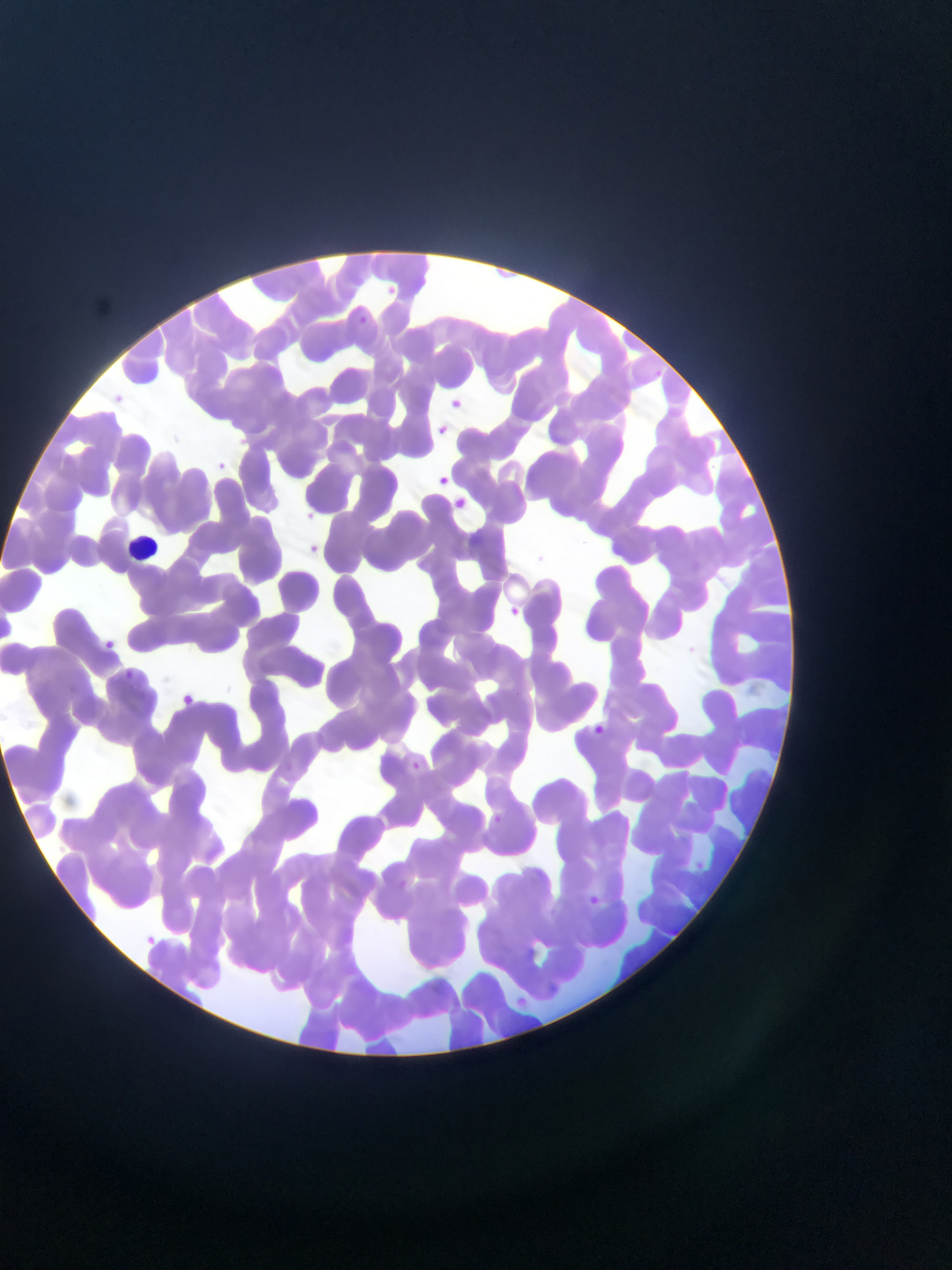
Approximate bounding boxes as left top right bottom in pixels.
Summary:
  - Leukocyte locations: 122 528 153 564
  - Malaria parasite locations: 388 282 399 293; 359 315 367 324; 651 364 663 381; 113 387 130 407; 445 396 462 408; 435 421 457 445; 237 432 251 444; 214 451 235 473; 436 472 448 482; 445 496 466 520; 300 508 326 526; 306 543 318 549; 506 605 515 616; 101 634 116 651; 125 670 135 679; 181 688 198 708; 592 720 604 738; 405 752 422 776; 490 812 501 820; 695 856 714 877; 395 878 412 891; 590 896 608 913; 545 905 565 916; 146 936 155 947; 522 940 543 961; 545 977 562 996; 515 994 531 1009
  - Field of view: single
  - Image size: 952×1270 pixels
  - Preparation: thin blood smear
  - Capture: mobile-phone photograph through a microscope
  - Country: Ghana